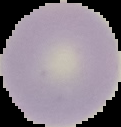
From a thin blood smear. Image is 121×127 pixels. Malaria status: uninfected. Cell region segmented out of the field of view; the surrounding area is masked to black.